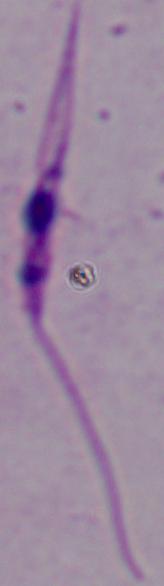

Summary:
  - Magnification: 1000x
  - Identification: Leishmania
  - Modality: photomicrograph